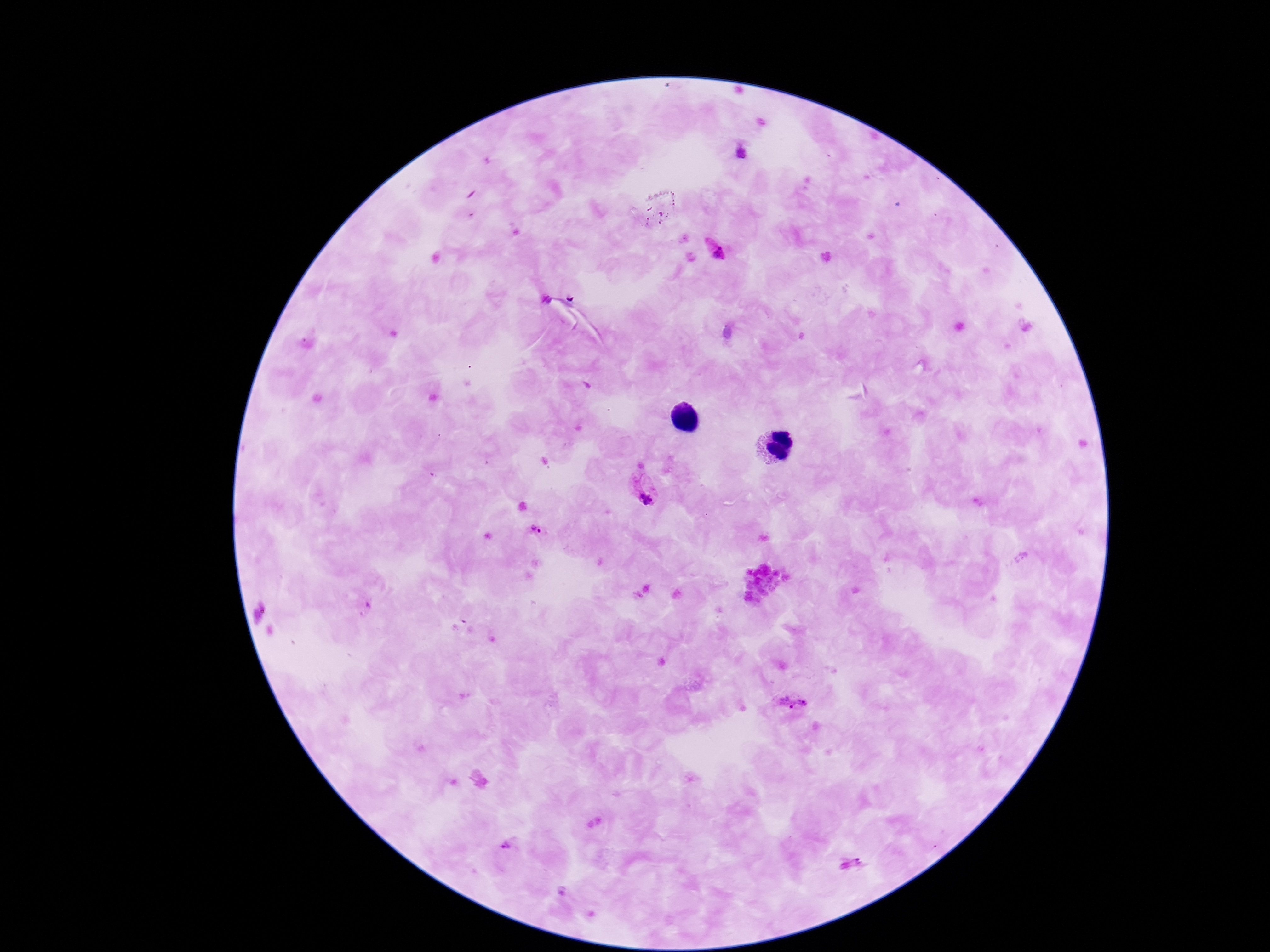
Approximate centers as [x, y] in pixels. Plasmodium parasite locations: [717, 251], [644, 491], [537, 530], [791, 702], [506, 848], [851, 866]. Image is 1270×952 pixels. One field from this slide. Giemsa stain. 100x magnification. Patient malaria status: infected. Thick peripheral-blood smear. Photographed through the microscope eyepiece with a smartphone camera.